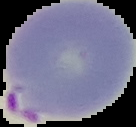
Result: malaria parasites identified. From a thin blood film. Image is 136×127 pixels. Segmented cell region on a black background.